Evaluate for malaria.
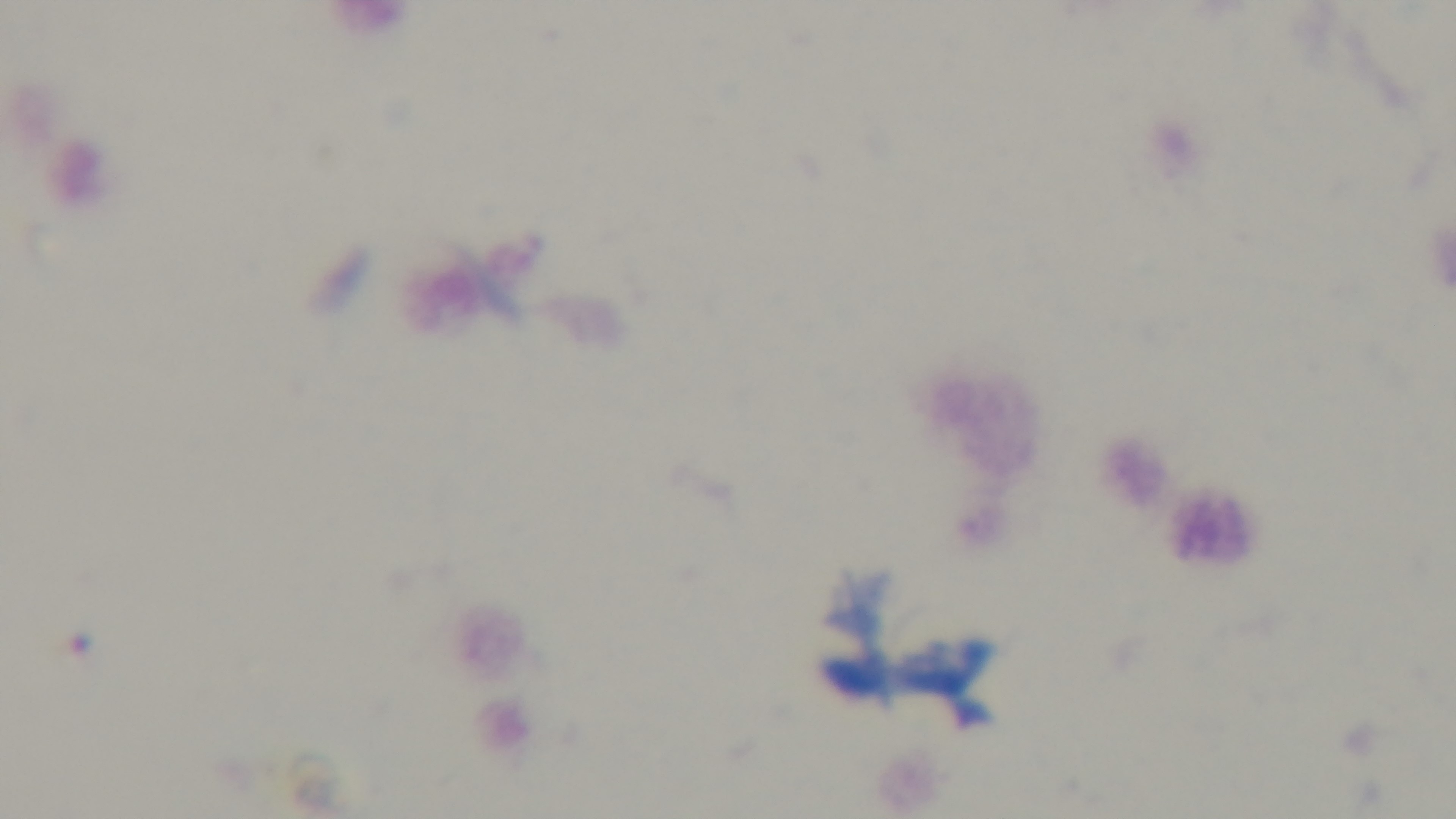

Negative.

Preparation: thick blood film. One field from the slide. Giemsa-stained. Light microscopy. 100x oil-immersion objective. Captured with a mounted 4K digital camera.